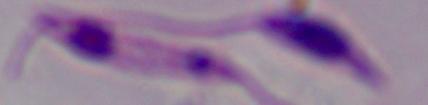

Summary:
  - Magnification: 1000x
  - Identification: Leishmania
  - Modality: photomicrograph